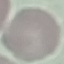 Malaria status: uninfected. Thin blood film. Cell patch, automatically extracted from a larger field of view and resized to 64 × 64 pixels. Giemsa-stained preparation. Acquired by smartphone through the microscope eyepiece.